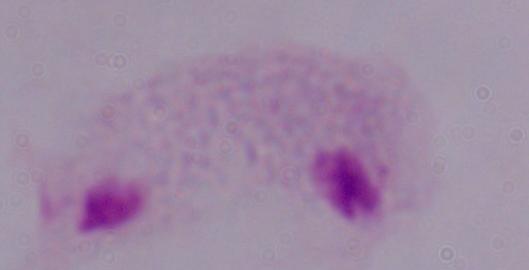 1000x magnification. Micrograph. A trichomonad is shown.